State which cell type is depicted.
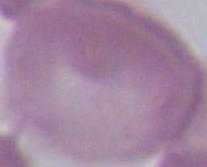
This is an erythrocyte.

1000x magnification. Photomicrograph.